Outline each blood parasite and name the species.
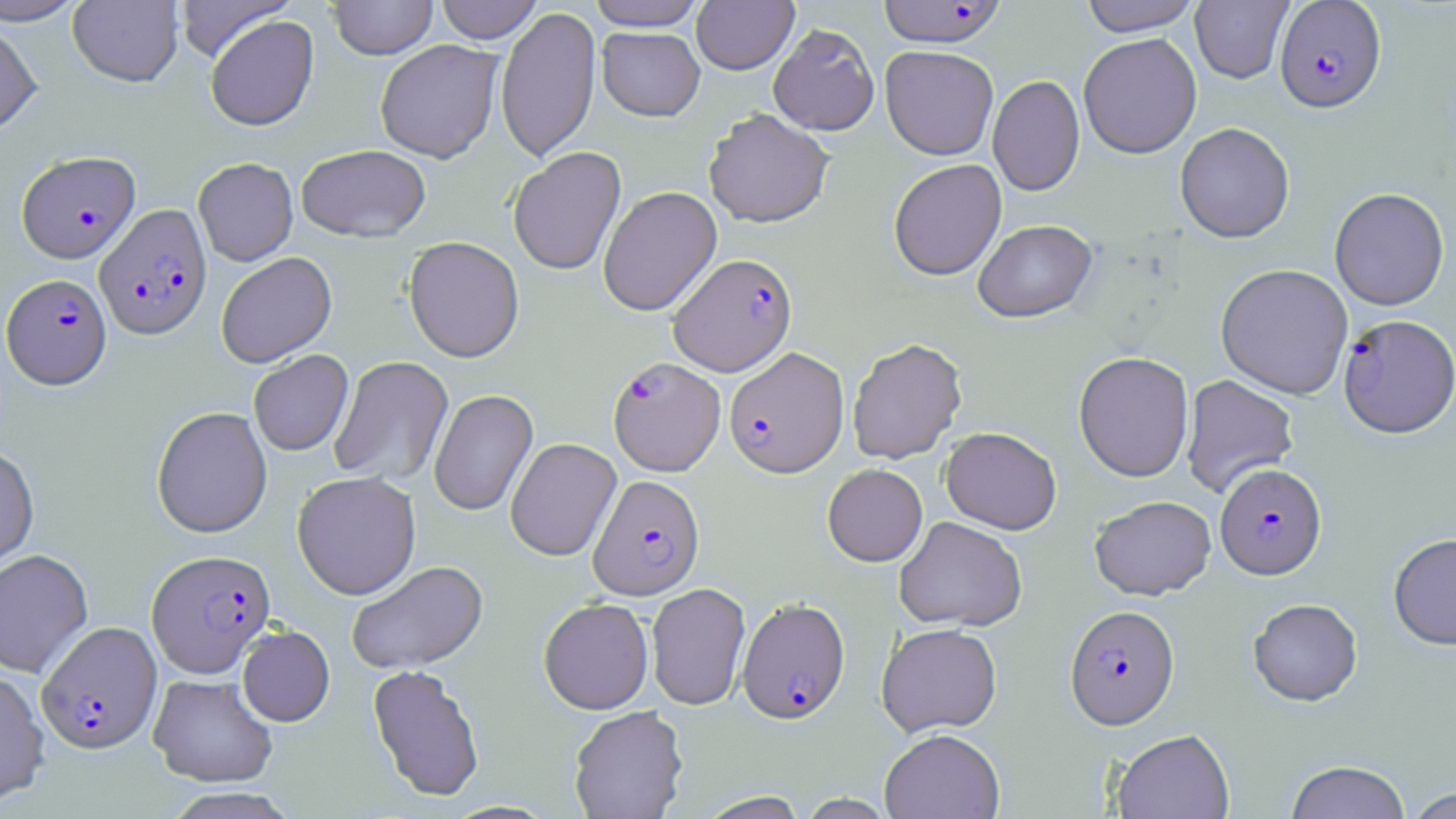
Approximate bounding boxes as named x1/y1/x2/y2 corners in pixels.
Plasmodium falciparum-infected red blood cells: (x1=877, y1=1, x2=1006, y2=47), (x1=1274, y1=1, x2=1386, y2=112), (x1=16, y1=150, x2=141, y2=263), (x1=95, y1=203, x2=212, y2=339), (x1=668, y1=252, x2=797, y2=376), (x1=2, y1=273, x2=112, y2=388), (x1=1338, y1=313, x2=1456, y2=439), (x1=724, y1=346, x2=849, y2=478), (x1=607, y1=356, x2=726, y2=476), (x1=1215, y1=462, x2=1326, y2=579), (x1=588, y1=474, x2=705, y2=600), (x1=146, y1=549, x2=275, y2=677), (x1=737, y1=597, x2=850, y2=723), (x1=1065, y1=604, x2=1179, y2=728), (x1=37, y1=621, x2=162, y2=753).
No Plasmodium ovale, Plasmodium malariae, Plasmodium vivax, Babesia divergens, or Trypanosoma brucei observed.

slide-level diagnosis = Plasmodium falciparum
image size = 1456×819 pixels
uninfected red blood cell locations = approximate bounding boxes as named x1/y1/x2/y2 corners in pixels: (x1=0, y1=0, x2=88, y2=25), (x1=173, y1=0, x2=292, y2=62), (x1=435, y1=0, x2=544, y2=44), (x1=587, y1=0, x2=707, y2=31), (x1=1079, y1=0, x2=1202, y2=36), (x1=1190, y1=0, x2=1293, y2=83), (x1=68, y1=1, x2=184, y2=87), (x1=328, y1=1, x2=437, y2=59), (x1=692, y1=1, x2=798, y2=74), (x1=495, y1=6, x2=601, y2=163), (x1=205, y1=14, x2=318, y2=131), (x1=0, y1=19, x2=43, y2=138), (x1=768, y1=23, x2=880, y2=135), (x1=597, y1=27, x2=705, y2=121), (x1=1078, y1=32, x2=1202, y2=159), (x1=375, y1=39, x2=503, y2=163), (x1=880, y1=45, x2=999, y2=160), (x1=988, y1=75, x2=1085, y2=196), (x1=704, y1=108, x2=834, y2=228), (x1=1175, y1=122, x2=1295, y2=243), (x1=296, y1=144, x2=430, y2=242), (x1=508, y1=147, x2=626, y2=276), (x1=193, y1=157, x2=298, y2=266), (x1=888, y1=158, x2=1007, y2=280), (x1=598, y1=186, x2=722, y2=316), (x1=1329, y1=187, x2=1449, y2=310), (x1=973, y1=219, x2=1097, y2=322), (x1=403, y1=236, x2=524, y2=362), (x1=216, y1=252, x2=337, y2=367), (x1=1215, y1=263, x2=1354, y2=399), (x1=847, y1=337, x2=967, y2=465), (x1=248, y1=350, x2=353, y2=456), (x1=1073, y1=351, x2=1194, y2=482), (x1=329, y1=355, x2=455, y2=487), (x1=1181, y1=375, x2=1299, y2=498), (x1=428, y1=389, x2=538, y2=517), (x1=151, y1=406, x2=272, y2=537), (x1=940, y1=426, x2=1062, y2=534), (x1=505, y1=437, x2=621, y2=560), (x1=0, y1=444, x2=39, y2=574), (x1=822, y1=463, x2=928, y2=567), (x1=292, y1=470, x2=421, y2=600), (x1=1090, y1=495, x2=1216, y2=599), (x1=894, y1=516, x2=1028, y2=631), (x1=1388, y1=532, x2=1456, y2=650), (x1=0, y1=549, x2=92, y2=678), (x1=346, y1=560, x2=488, y2=674), (x1=646, y1=582, x2=750, y2=710), (x1=538, y1=598, x2=653, y2=714), (x1=1248, y1=598, x2=1363, y2=705), (x1=876, y1=622, x2=1002, y2=737), (x1=237, y1=625, x2=335, y2=726), (x1=367, y1=664, x2=485, y2=802), (x1=0, y1=668, x2=50, y2=808), (x1=148, y1=673, x2=278, y2=787), (x1=568, y1=705, x2=688, y2=819), (x1=879, y1=728, x2=1004, y2=819), (x1=1111, y1=729, x2=1234, y2=819), (x1=1285, y1=760, x2=1411, y2=819), (x1=159, y1=787, x2=302, y2=818), (x1=1405, y1=787, x2=1454, y2=819)
field of view = one of a larger specimen
modality = light microscopy
magnification = 1000x
stain = May-Grünwald-Giemsa
preparation = thin blood film